State which cell type is depicted.
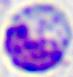

A leukocyte.

Summary:
  - Magnification: 400x
  - Modality: micrograph